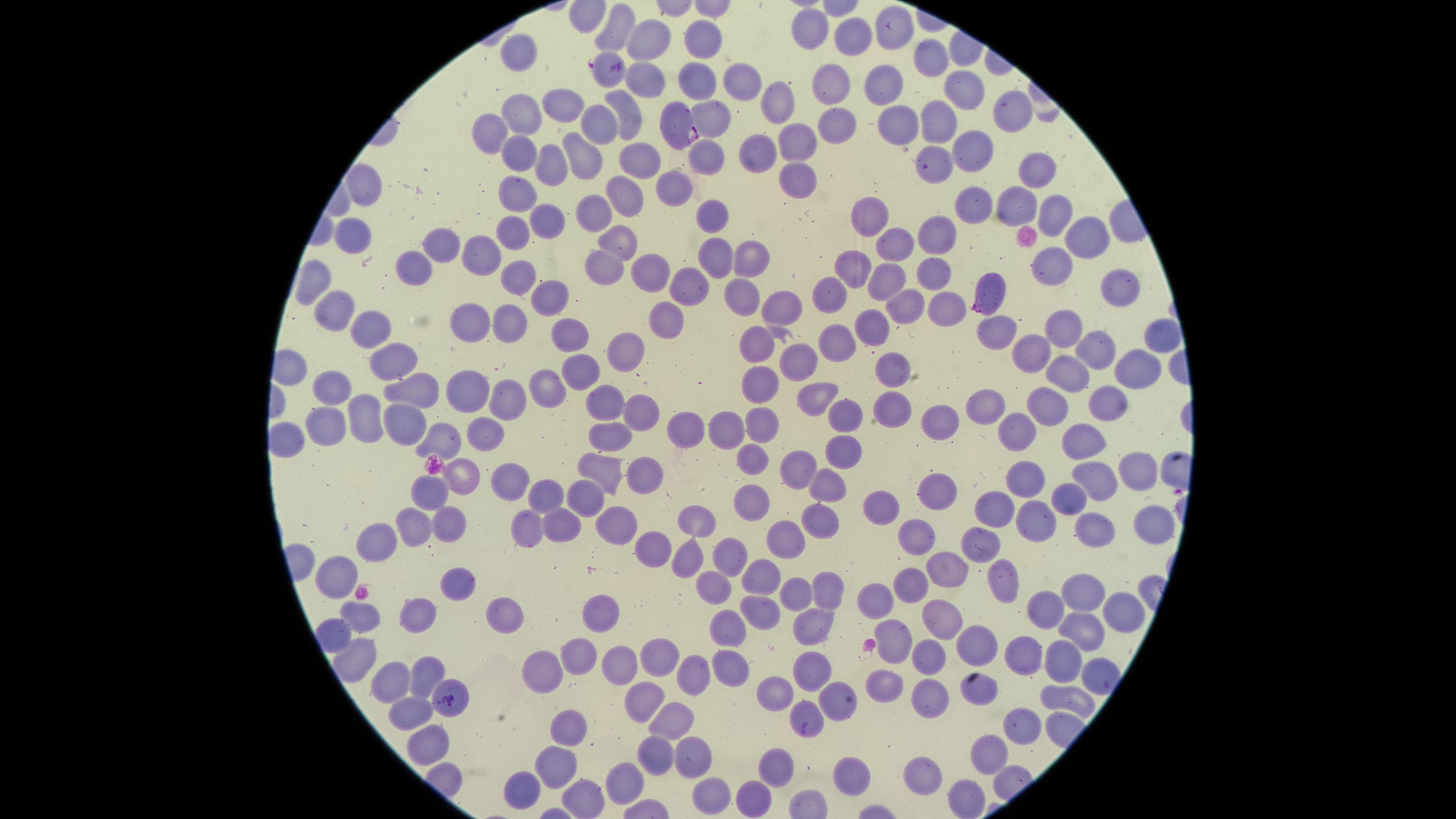

field of view = single
capture = smartphone photograph through the microscope eyepiece
stain = Giemsa
uninfected red blood cells = approximate marker points as [x, y] in pixels: [619, 27], [883, 27], [806, 35], [648, 38], [701, 45], [857, 45], [928, 59], [518, 60], [731, 75], [885, 77], [642, 81], [696, 82], [827, 84], [966, 88], [780, 105], [525, 109], [570, 109], [627, 110], [1005, 110], [712, 116], [839, 119], [492, 122], [606, 123], [942, 124], [797, 134], [899, 134], [973, 145], [522, 149], [764, 150], [582, 151], [708, 152], [636, 160], [550, 166], [1035, 171], [936, 172], [798, 177], [680, 182], [624, 194], [360, 196], [520, 201], [1021, 201], [977, 209], [1048, 212], [594, 216], [713, 216], [552, 221], [869, 222], [514, 232], [615, 236], [938, 236], [351, 240], [1084, 240], [450, 244], [489, 249], [893, 252], [712, 258], [750, 260], [410, 263], [857, 264], [603, 267], [654, 272], [928, 272], [1048, 273], [514, 275], [313, 280], [889, 284], [1117, 284], [690, 286], [740, 294], [329, 300], [827, 301], [558, 303], [787, 303], [908, 304], [942, 308], [670, 319], [472, 323], [1060, 323], [510, 324], [363, 325], [872, 328], [570, 331], [990, 333], [1153, 336], [835, 341], [751, 348], [630, 350], [1034, 354], [1089, 355], [397, 361], [805, 364], [1139, 366], [582, 367], [898, 370], [1070, 374], [765, 384], [546, 385], [336, 389], [473, 390], [416, 392], [819, 398], [1048, 401], [499, 402], [604, 402], [901, 407], [979, 407], [1112, 407], [642, 410], [845, 416], [367, 417], [944, 420], [412, 423], [761, 423], [327, 424], [688, 426], [1021, 432], [731, 433], [487, 439], [612, 439], [446, 441], [1078, 441], [839, 454], [752, 457], [596, 464], [1133, 466], [643, 470], [459, 473], [795, 473], [1033, 480], [829, 481], [1092, 481], [513, 483], [937, 483], [429, 491], [590, 493], [544, 494], [1070, 495], [755, 499], [1000, 502], [884, 506], [705, 520], [815, 521], [1037, 523], [1149, 523], [451, 524], [617, 524], [1095, 524], [557, 527], [533, 529], [413, 532], [920, 533], [989, 538], [652, 543], [788, 543], [380, 550], [727, 552], [689, 561], [945, 569], [1000, 575], [343, 576], [763, 581], [458, 582], [913, 582], [710, 586], [1088, 588], [828, 593], [794, 594], [884, 595], [504, 606], [604, 606], [1046, 606], [1122, 608], [763, 615], [422, 616], [936, 618], [365, 624], [810, 625], [1083, 630], [727, 632], [896, 635], [329, 638], [964, 643], [577, 655], [1024, 655], [1066, 655], [350, 658], [923, 658], [663, 660], [620, 662], [812, 666], [429, 667], [729, 669], [542, 674], [696, 678], [391, 681], [886, 684], [778, 693], [931, 694], [836, 695], [1071, 698], [636, 703], [415, 714], [809, 714], [1022, 720], [666, 726], [564, 729], [436, 747], [653, 753], [995, 754], [695, 755], [779, 758], [558, 762], [636, 775], [856, 776], [929, 777], [523, 785], [716, 793], [759, 795], [588, 798], [969, 800]
presence = malaria parasites detected
parasitized red blood cells = approximate marker points as [x, y] in pixels: [608, 69], [677, 122], [985, 292], [454, 695]
image size = 1456×819 pixels
visible region = circular
preparation = thin blood smear
species = Plasmodium falciparum